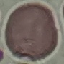
result = no malaria parasites seen
image type = cell patch, automatically extracted from a larger field of view and resized to 64 × 64 pixels
preparation = thin blood smear
capture = smartphone through the microscope eyepiece
stain = Giemsa